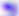

Summary:
  - Identification: Toxoplasma gondii
  - Modality: photomicrograph
  - Magnification: 400x